Assess the morphology of the red blood cells.
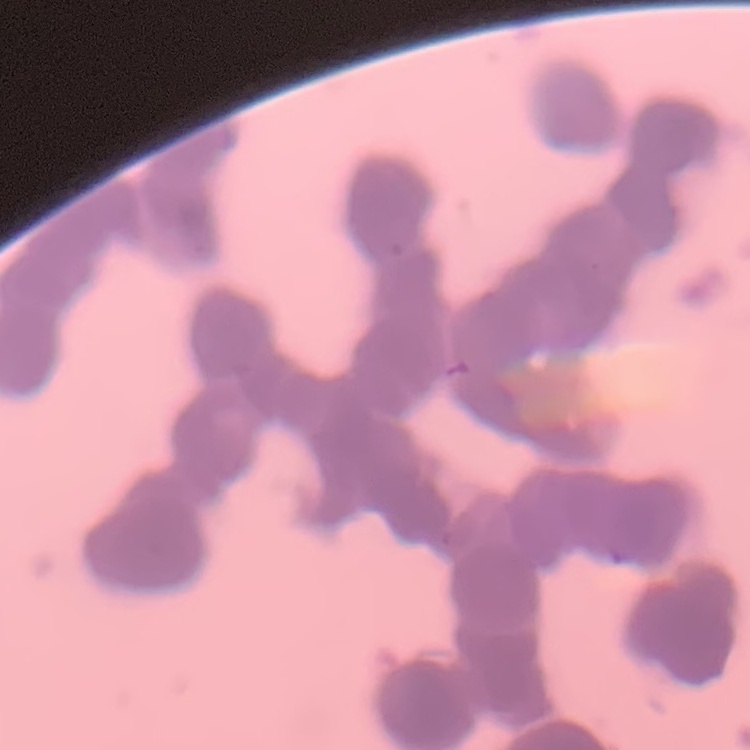

They show rouleaux formation.

Summary:
  - Preparation: thin blood smear
  - Stain: Field's or Giemsa
  - Image type: square crop of a larger photomicrograph